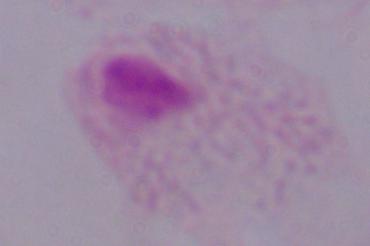
identification: trichomonad
modality: micrograph
magnification: 1000x